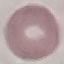
Result: no malaria parasites seen. Thin smear of blood. Giemsa-stained preparation. Cell patch, automatically extracted from a larger field of view and resized to 64 × 64 pixels. Acquired by smartphone through the microscope eyepiece.